Identify the cell.
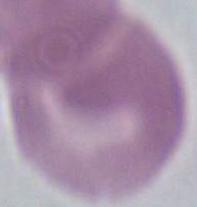

An erythrocyte.

magnification = 1000x
modality = photomicrograph